Outline each blood parasite and name the species.
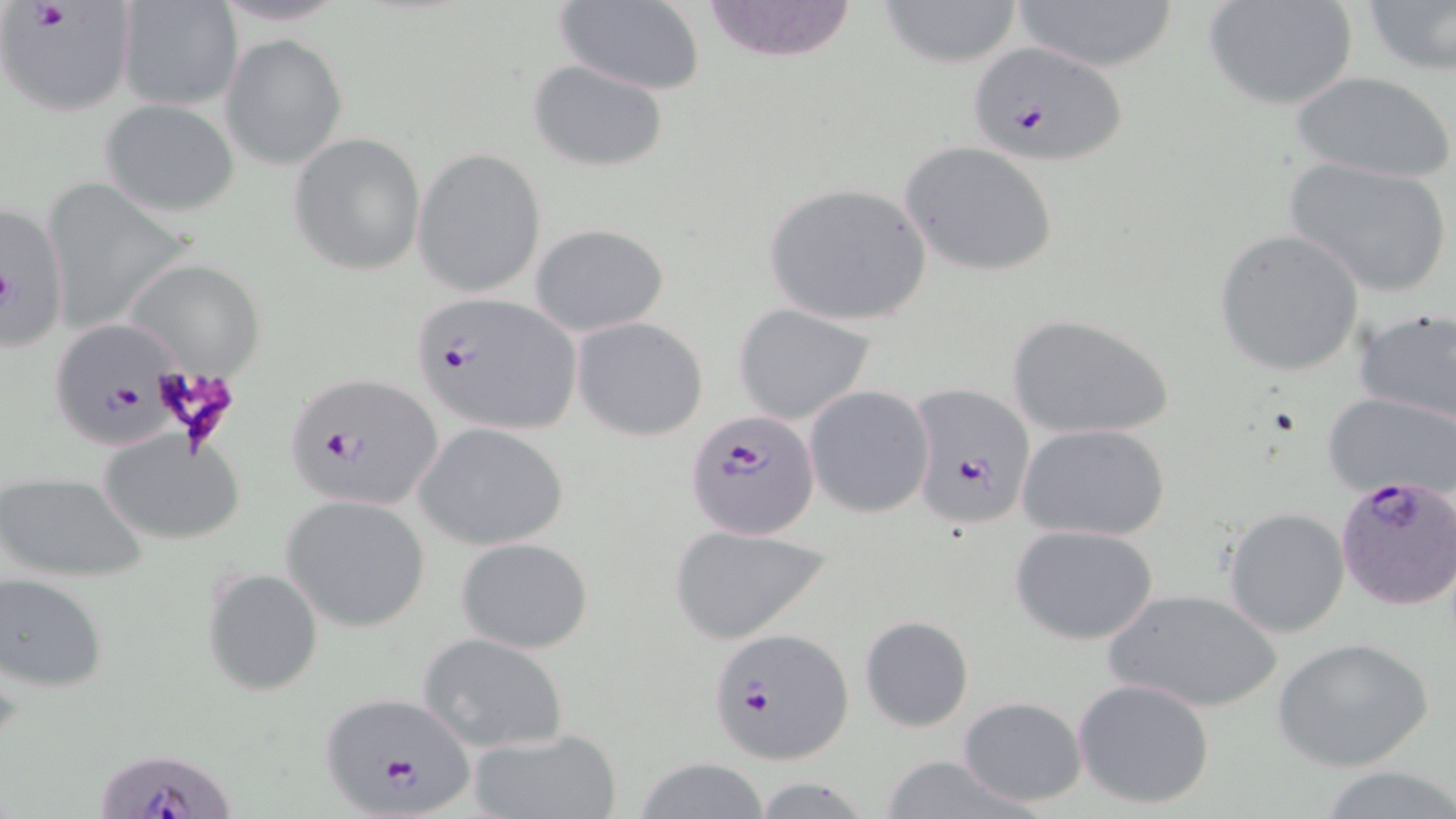

Approximate bounding boxes as [x1, y1, x2, y2] in pixels.
Plasmodium falciparum-infected red blood cells: [0, 2, 135, 116], [965, 40, 1132, 164], [409, 292, 588, 437], [48, 323, 184, 445], [282, 372, 446, 511], [907, 383, 1038, 527], [685, 408, 819, 540], [1335, 472, 1455, 613], [706, 627, 853, 764], [319, 690, 480, 813], [94, 743, 234, 819].
No Plasmodium ovale, Plasmodium malariae, Plasmodium vivax, Babesia divergens, or Trypanosoma brucei observed.

Uninfected red blood cell locations: [698, 0, 861, 64], [875, 0, 1026, 68], [1013, 0, 1179, 73], [1202, 0, 1359, 112], [549, 1, 706, 94], [117, 2, 242, 111], [1360, 2, 1456, 78], [221, 34, 347, 169], [527, 58, 670, 172], [1289, 70, 1454, 184], [99, 99, 240, 218], [288, 133, 426, 276], [899, 140, 1060, 278], [412, 147, 547, 299], [1283, 155, 1454, 299], [762, 179, 935, 327], [0, 198, 70, 350], [531, 223, 669, 336], [1212, 229, 1365, 378], [119, 256, 269, 380], [731, 301, 879, 427], [1352, 307, 1456, 425], [1005, 312, 1175, 440], [573, 316, 709, 441], [804, 384, 934, 518], [1322, 391, 1456, 500], [1017, 421, 1173, 541], [415, 422, 569, 550], [98, 431, 245, 547], [1, 470, 150, 583], [282, 495, 431, 631], [1223, 507, 1350, 637], [1009, 523, 1159, 645], [668, 524, 831, 645], [455, 536, 594, 653], [202, 566, 323, 697], [0, 572, 110, 693], [1103, 588, 1284, 714], [859, 614, 974, 733], [420, 633, 570, 754], [1274, 636, 1435, 773], [1072, 678, 1216, 810], [956, 695, 1089, 808], [468, 727, 621, 819], [878, 753, 1033, 819], [631, 758, 775, 818], [1315, 765, 1456, 819], [749, 776, 878, 817]. Slide-level diagnosis: Plasmodium falciparum. Image is 1456×819 pixels. Light microscopy. Captured at 1000x magnification. May-Grünwald-Giemsa-stained preparation. Thin blood smear. One field of a larger specimen.